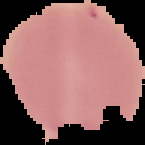
Summary:
  - Result: no malaria parasites seen
  - Image type: cell region segmented out of the field of view; surrounding area masked to black
  - Preparation: thin blood smear
  - Image size: 145×145 pixels